Report the malaria status of this cell.
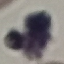
Uninfected.

Cell patch, automatically extracted from a larger field of view and resized to 64 × 64 pixels. Thin smear of blood. Acquired by smartphone through the microscope eyepiece. Giemsa stain.